Outline each blood parasite and name the species.
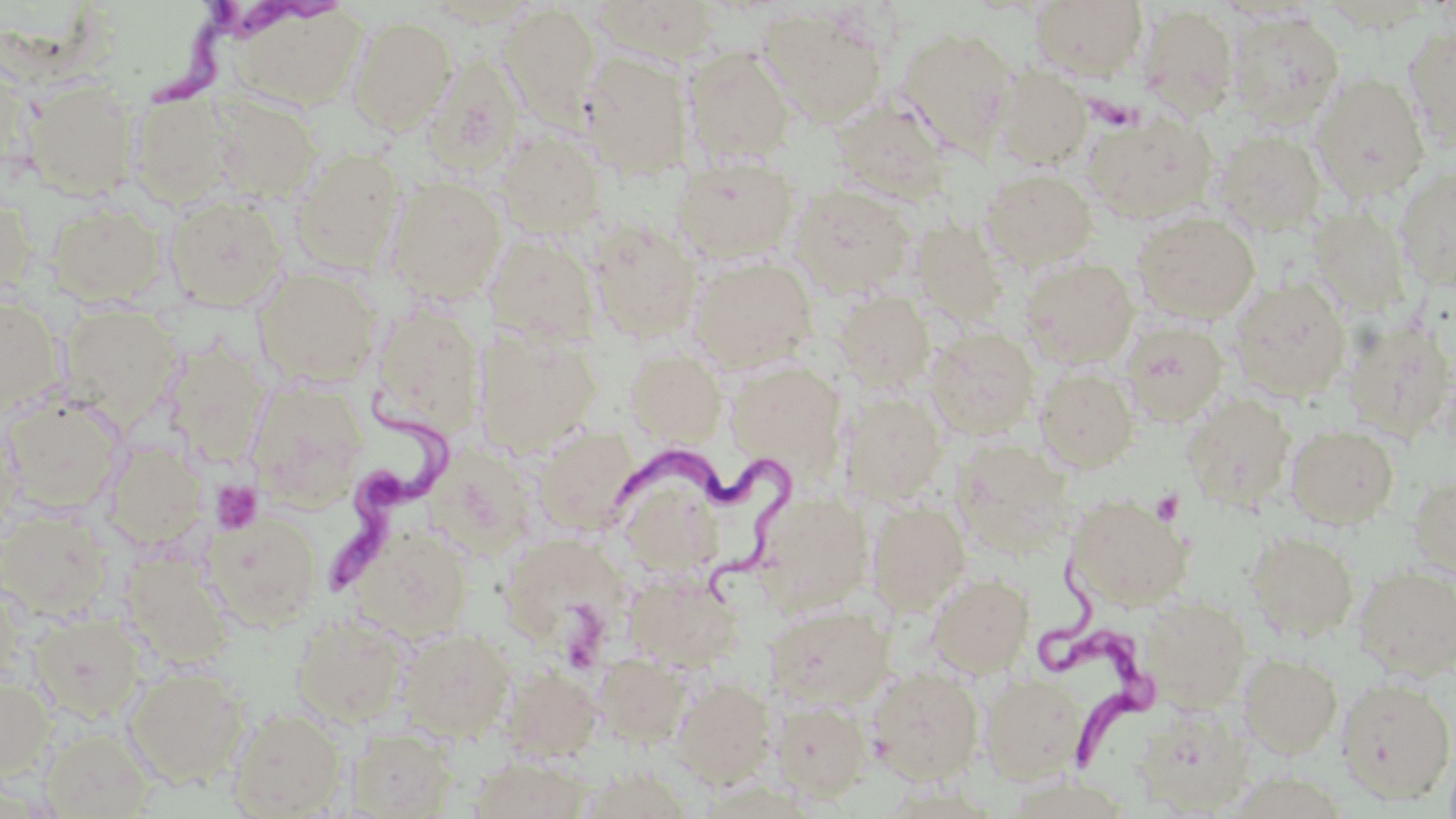
Approximate bounding boxes as named x1/y1/x2/y2 corners in pixels.
Trypanosoma brucei: (x1=145, y1=2, x2=331, y2=116), (x1=318, y1=389, x2=467, y2=611), (x1=614, y1=447, x2=800, y2=608), (x1=1051, y1=561, x2=1149, y2=776).
No Plasmodium falciparum, Plasmodium ovale, Plasmodium malariae, Plasmodium vivax, or Babesia divergens observed.

slide-level diagnosis = Trypanosoma brucei
magnification = 1000x
stain = May-Grünwald-Giemsa
preparation = thin blood smear
modality = optical microscopy
field of view = one of a larger specimen
image size = 1456×819 pixels
uninfected red blood cell locations = approximate bounding boxes as named x1/y1/x2/y2 corners in pixels: (x1=591, y1=0, x2=722, y2=65), (x1=1030, y1=0, x2=1148, y2=81), (x1=419, y1=2, x2=542, y2=29), (x1=226, y1=3, x2=368, y2=112), (x1=498, y1=3, x2=600, y2=125), (x1=1138, y1=4, x2=1239, y2=120), (x1=759, y1=6, x2=889, y2=127), (x1=1226, y1=8, x2=1344, y2=127), (x1=347, y1=15, x2=457, y2=134), (x1=896, y1=25, x2=1017, y2=154), (x1=1403, y1=26, x2=1455, y2=151), (x1=683, y1=47, x2=795, y2=164), (x1=581, y1=50, x2=693, y2=179), (x1=0, y1=56, x2=38, y2=181), (x1=420, y1=56, x2=524, y2=176), (x1=993, y1=65, x2=1092, y2=169), (x1=1311, y1=72, x2=1430, y2=201), (x1=23, y1=79, x2=140, y2=200), (x1=127, y1=91, x2=234, y2=207), (x1=206, y1=93, x2=322, y2=202), (x1=831, y1=94, x2=954, y2=203), (x1=1083, y1=109, x2=1216, y2=224), (x1=1213, y1=128, x2=1327, y2=234), (x1=497, y1=130, x2=606, y2=238), (x1=289, y1=148, x2=402, y2=274), (x1=674, y1=156, x2=799, y2=264), (x1=1394, y1=164, x2=1456, y2=292), (x1=981, y1=169, x2=1098, y2=270), (x1=385, y1=176, x2=507, y2=303), (x1=790, y1=184, x2=914, y2=297), (x1=0, y1=189, x2=36, y2=300), (x1=164, y1=194, x2=288, y2=311), (x1=46, y1=202, x2=166, y2=305), (x1=1308, y1=206, x2=1411, y2=316), (x1=1133, y1=212, x2=1260, y2=323), (x1=910, y1=218, x2=1009, y2=326), (x1=588, y1=219, x2=702, y2=341), (x1=484, y1=233, x2=599, y2=345), (x1=1020, y1=256, x2=1140, y2=367), (x1=690, y1=257, x2=816, y2=372), (x1=253, y1=267, x2=382, y2=388), (x1=1229, y1=277, x2=1352, y2=402), (x1=833, y1=290, x2=935, y2=391), (x1=0, y1=295, x2=67, y2=419), (x1=369, y1=304, x2=485, y2=438), (x1=60, y1=305, x2=181, y2=426), (x1=1343, y1=316, x2=1455, y2=443), (x1=1119, y1=321, x2=1228, y2=426), (x1=474, y1=326, x2=601, y2=456), (x1=925, y1=326, x2=1039, y2=439), (x1=162, y1=342, x2=269, y2=468), (x1=624, y1=347, x2=726, y2=446), (x1=725, y1=361, x2=846, y2=475), (x1=1036, y1=366, x2=1140, y2=472), (x1=246, y1=379, x2=371, y2=508), (x1=841, y1=392, x2=947, y2=504), (x1=1182, y1=393, x2=1294, y2=509), (x1=2, y1=394, x2=126, y2=513), (x1=1286, y1=424, x2=1399, y2=528), (x1=532, y1=425, x2=640, y2=534), (x1=104, y1=440, x2=207, y2=550), (x1=959, y1=442, x2=1081, y2=558), (x1=425, y1=446, x2=538, y2=558), (x1=615, y1=466, x2=726, y2=579), (x1=1409, y1=472, x2=1456, y2=580), (x1=752, y1=490, x2=875, y2=611), (x1=1066, y1=494, x2=1191, y2=610), (x1=867, y1=501, x2=970, y2=614), (x1=1, y1=509, x2=112, y2=617), (x1=204, y1=511, x2=322, y2=629), (x1=350, y1=524, x2=472, y2=643), (x1=499, y1=531, x2=633, y2=654), (x1=1245, y1=531, x2=1359, y2=642), (x1=120, y1=551, x2=235, y2=670), (x1=1353, y1=565, x2=1456, y2=679), (x1=625, y1=571, x2=742, y2=671), (x1=929, y1=573, x2=1034, y2=677), (x1=1142, y1=595, x2=1251, y2=710), (x1=764, y1=603, x2=892, y2=709), (x1=292, y1=613, x2=410, y2=727), (x1=31, y1=614, x2=143, y2=723), (x1=398, y1=628, x2=514, y2=741), (x1=593, y1=651, x2=692, y2=747), (x1=1239, y1=653, x2=1342, y2=758), (x1=867, y1=665, x2=984, y2=785), (x1=123, y1=666, x2=249, y2=788), (x1=499, y1=666, x2=602, y2=761), (x1=981, y1=672, x2=1089, y2=783), (x1=0, y1=674, x2=55, y2=778), (x1=1335, y1=676, x2=1455, y2=804), (x1=673, y1=678, x2=777, y2=787), (x1=772, y1=700, x2=872, y2=803), (x1=1134, y1=704, x2=1254, y2=814), (x1=226, y1=707, x2=346, y2=818), (x1=39, y1=727, x2=157, y2=818), (x1=348, y1=727, x2=457, y2=818), (x1=470, y1=755, x2=591, y2=818), (x1=577, y1=764, x2=695, y2=818)
platelet locations = approximate bounding boxes as named x1/y1/x2/y2 corners in pixels: (x1=210, y1=481, x2=262, y2=535), (x1=1151, y1=489, x2=1185, y2=526)